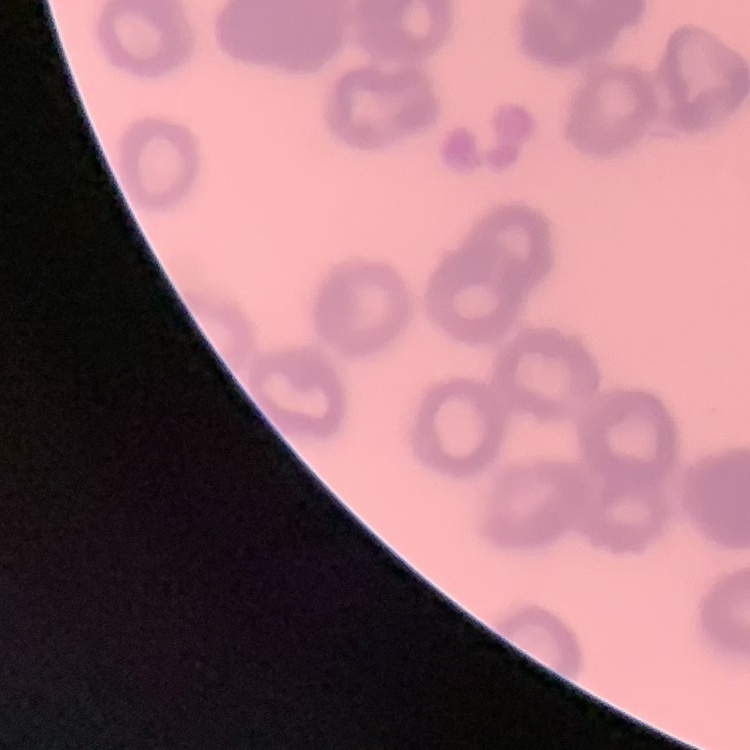
erythrocyte morphology = rouleaux formation
preparation = thin blood film
stain = Field's or Giemsa
image type = square crop of a larger photomicrograph